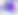

magnification = 400x
identification = Toxoplasma gondii
modality = micrograph